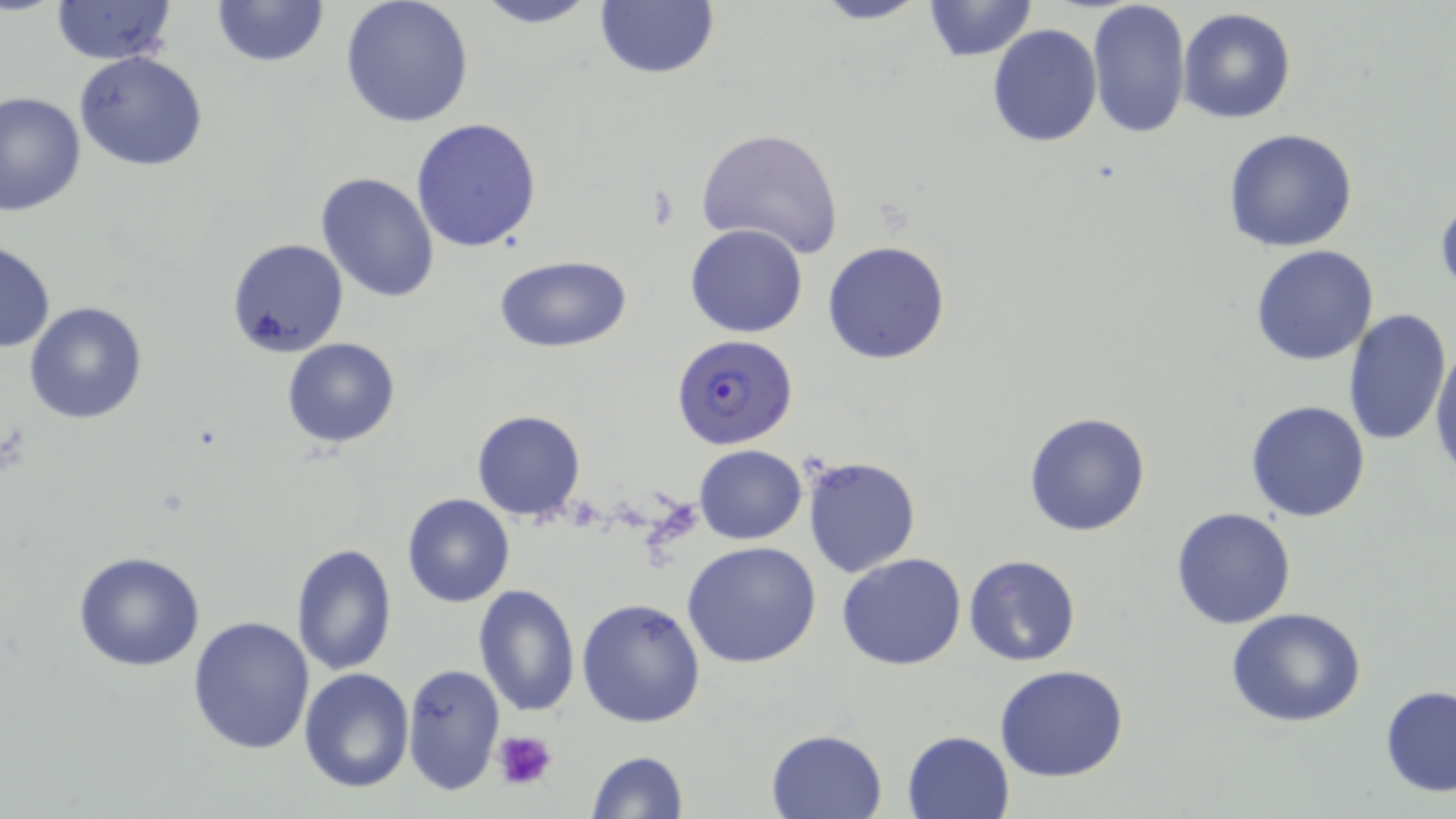
{
  "slide_level_diagnosis": "Plasmodium falciparum",
  "preparation": "thin blood film",
  "platelet_locations": "approximate bounding boxes as (x1,y1)-(x2,y2) corner pairs in pixels: (492,730)-(555,789)",
  "uninfected_red_blood_cell_locations": "approximate bounding boxes as (x1,y1)-(x2,y2) corner pairs in pixels: (470,0)-(604,28), (805,0)-(934,25), (922,0)-(1039,61), (1087,0)-(1192,140), (48,1)-(180,65), (209,1)-(329,69), (340,1)-(476,127), (595,1)-(720,79), (1176,7)-(1296,125), (987,24)-(1102,148), (73,51)-(208,172), (0,90)-(86,215), (409,117)-(542,254), (695,127)-(845,261), (1222,128)-(1358,252), (315,171)-(439,304), (1434,192)-(1456,298), (686,223)-(808,339), (226,236)-(347,356), (0,240)-(54,353), (822,241)-(951,365), (1251,245)-(1380,366), (495,254)-(631,353), (25,301)-(147,424), (1342,308)-(1451,447), (282,337)-(401,448), (1428,341)-(1455,481), (1243,399)-(1371,522), (471,409)-(586,522), (1023,412)-(1151,537), (694,445)-(806,544), (801,455)-(921,577), (401,493)-(516,608), (1170,507)-(1296,629), (682,540)-(822,668), (289,542)-(398,677), (72,551)-(206,671), (836,553)-(968,672), (964,554)-(1080,667), (471,584)-(580,718), (576,597)-(706,728), (1225,607)-(1368,728), (187,615)-(316,757), (402,662)-(505,796), (994,664)-(1130,783), (299,667)-(413,792), (1380,685)-(1456,797), (766,728)-(887,818), (901,730)-(1016,819), (584,750)-(688,819)",
  "plasmodium_falciparum_infected_red_blood_cell_locations": "approximate bounding boxes as (x1,y1)-(x2,y2) corner pairs in pixels: (673,342)-(799,455)",
  "stain": "May-Grünwald-Giemsa",
  "modality": "optical microscopy",
  "image_size": "1456×819 pixels",
  "magnification": "1000x",
  "field_of_view": "one of a larger specimen"
}